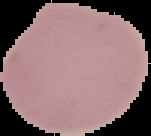
Summary:
  - Image size: 151×136 pixels
  - Preparation: thin blood smear
  - Result: negative for malaria parasites
  - Image type: cell region segmented out of the field of view; surrounding area masked to black